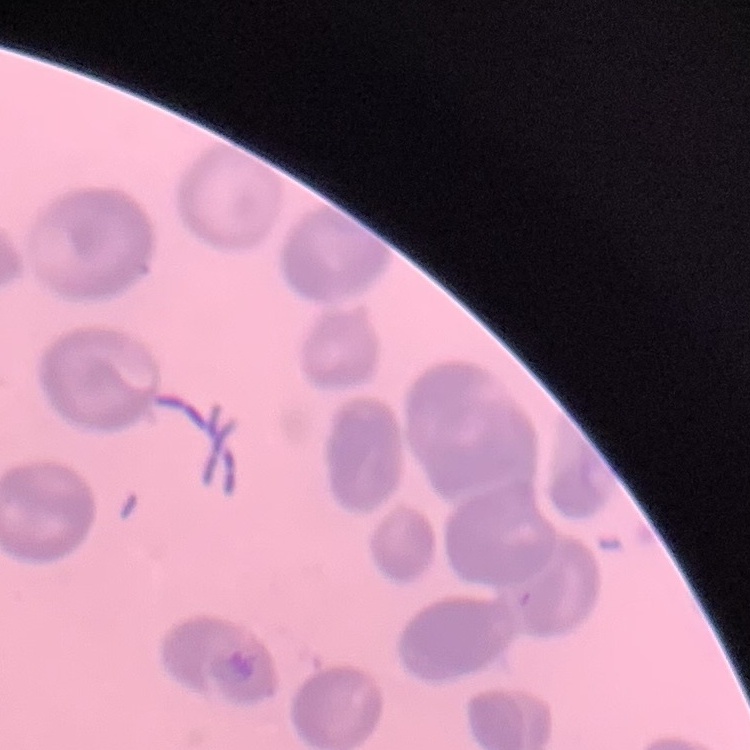
{
  "red_blood_cell_morphology": "no rouleaux formation",
  "image_type": "square crop of a larger photomicrograph",
  "stain": "Field's or Giemsa",
  "preparation": "thin peripheral smear"
}